Report the malaria status of this cell.
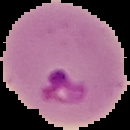
Parasitized.

preparation = thin blood smear
image type = cell region segmented out of the field of view; surrounding area masked to black
image size = 130×130 pixels